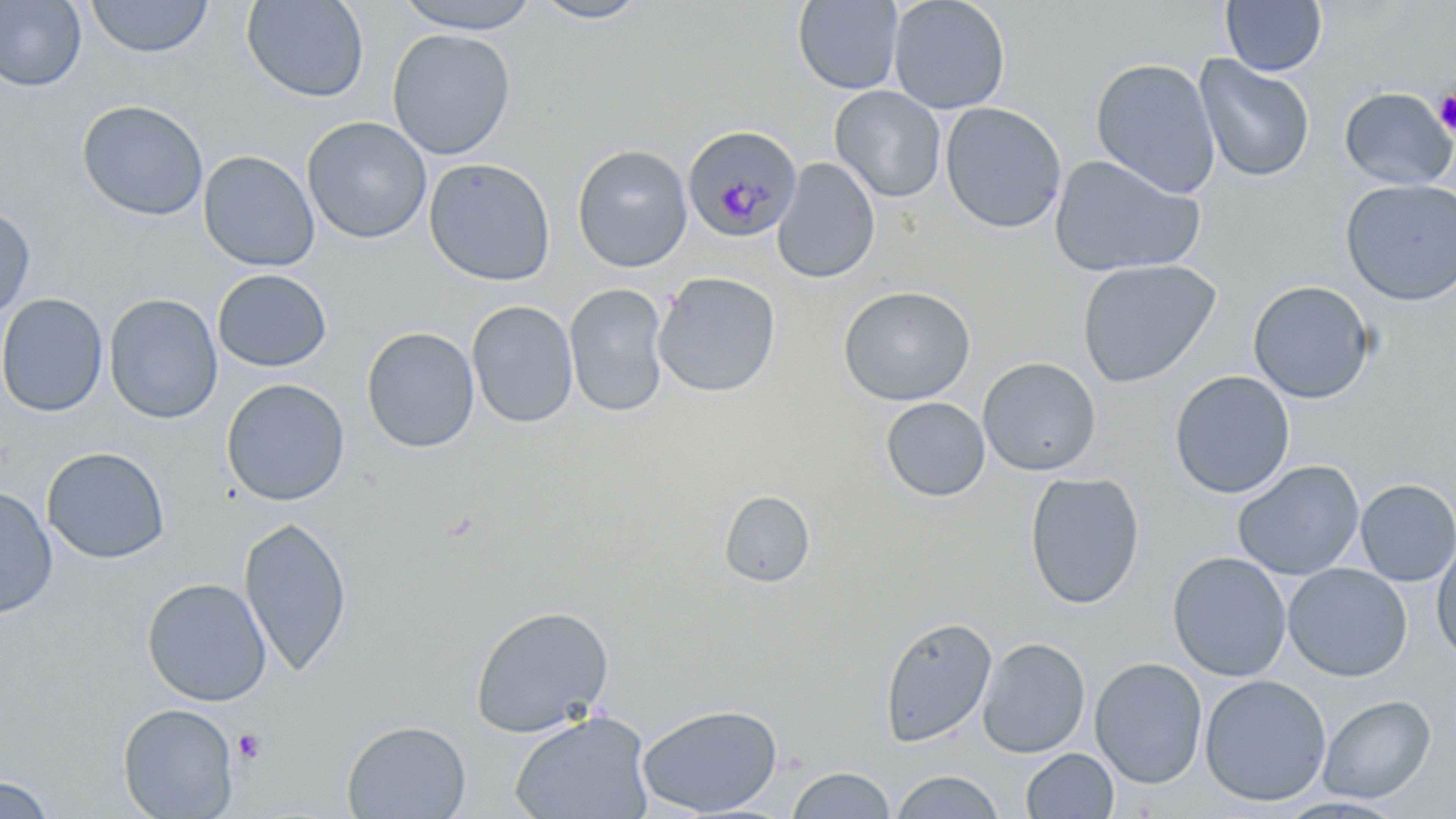

Summary:
  - Coordinate format: approximate bounding boxes as (x1, y1, x2, y2) in pixels
  - Platelet locations: (1434, 91, 1456, 137), (233, 728, 267, 765)
  - Plasmodium malariae-infected red blood cell locations: (682, 126, 806, 243)
  - Uninfected red blood cell locations: (86, 0, 214, 59), (241, 0, 369, 103), (391, 0, 545, 34), (888, 0, 1011, 114), (0, 1, 87, 92), (528, 1, 652, 25), (792, 1, 904, 94), (1220, 1, 1328, 76), (386, 28, 516, 160), (1193, 55, 1315, 182), (1090, 58, 1220, 198), (829, 85, 947, 202), (1339, 87, 1456, 191), (76, 98, 210, 221), (939, 102, 1067, 234), (301, 115, 433, 244), (572, 144, 693, 273), (198, 150, 319, 271), (1048, 154, 1206, 279), (423, 157, 556, 286), (772, 157, 881, 284), (1340, 178, 1456, 305), (0, 208, 36, 321), (1076, 258, 1222, 388), (212, 269, 332, 373), (652, 272, 781, 397), (1247, 280, 1376, 403), (564, 283, 669, 418), (837, 285, 976, 406), (0, 293, 108, 417), (103, 293, 223, 424), (466, 300, 579, 428), (361, 326, 480, 453), (977, 356, 1102, 477), (1170, 370, 1295, 499), (221, 378, 350, 506), (880, 397, 991, 502), (41, 445, 171, 564), (1232, 460, 1365, 581), (1024, 471, 1145, 610), (1355, 479, 1456, 586), (0, 487, 58, 618), (718, 490, 815, 588), (238, 515, 352, 676), (1431, 537, 1456, 663), (1167, 551, 1292, 682), (1282, 563, 1412, 682), (141, 577, 272, 706), (469, 604, 614, 738), (878, 616, 997, 748), (976, 637, 1091, 758), (1089, 657, 1208, 789), (1199, 674, 1332, 806), (1317, 695, 1436, 803), (117, 703, 239, 818), (636, 703, 783, 817), (508, 709, 655, 819), (342, 719, 472, 818), (1021, 748, 1119, 819), (786, 766, 895, 819), (890, 770, 1005, 818), (1, 774, 55, 819), (1274, 794, 1409, 817)
  - Slide-level diagnosis: Plasmodium malariae
  - Preparation: thin blood smear
  - Modality: optical microscopy
  - Stain: May-Grünwald-Giemsa
  - Image size: 1456×819 pixels
  - Field of view: one of a larger specimen
  - Magnification: 1000x